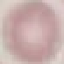

Malaria status: uninfected. Giemsa-stained preparation. Thin blood film. Cell patch, automatically extracted from a larger field of view and resized to 64 × 64 pixels. Acquired by smartphone through the microscope eyepiece.